State which cell type is depicted.
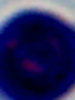
This is a leukocyte.

Summary:
  - Magnification: 1000x
  - Modality: micrograph